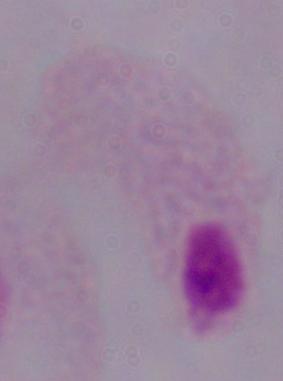
modality = photomicrograph
magnification = 1000x
identification = trichomonad